Describe the morphology of the erythrocytes.
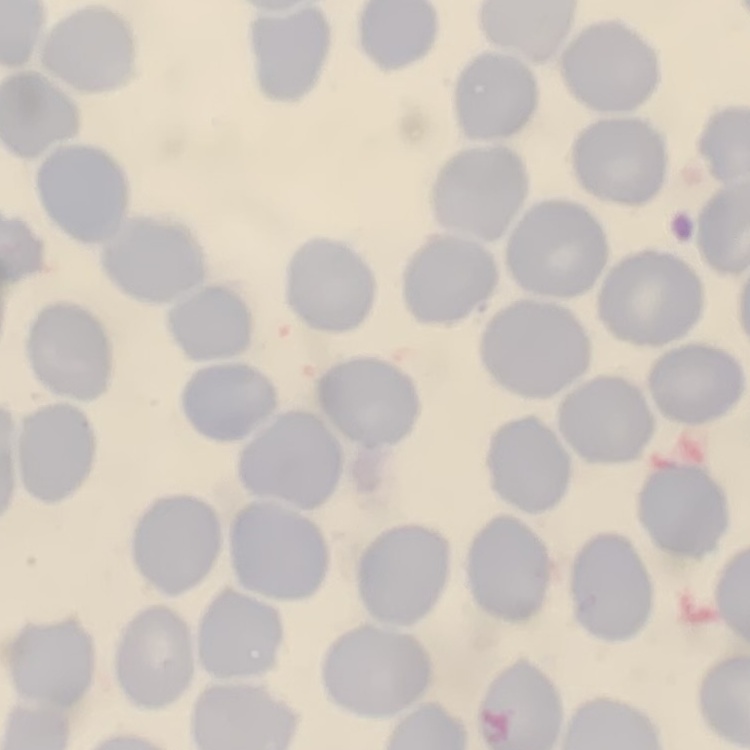

They show no rouleaux formation.

Summary:
  - Preparation: thin peripheral smear
  - Stain: Field's or Giemsa
  - Image type: square crop of a larger photomicrograph